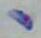
identification = Toxoplasma gondii
modality = micrograph
magnification = 1000x